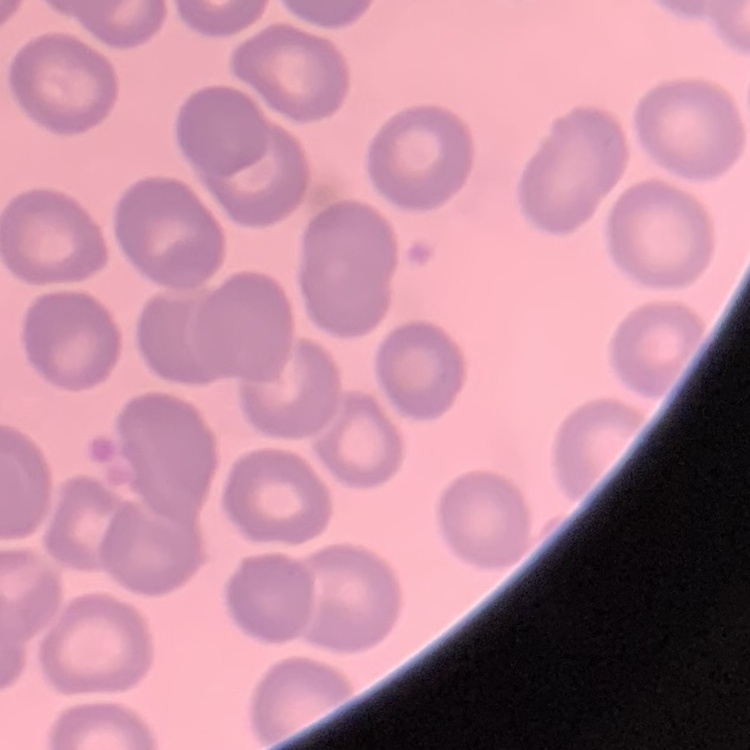

erythrocyte_morphology: no rouleaux formation
stain: Field's or Giemsa
image_type: square crop of a larger photomicrograph
preparation: thin blood smear